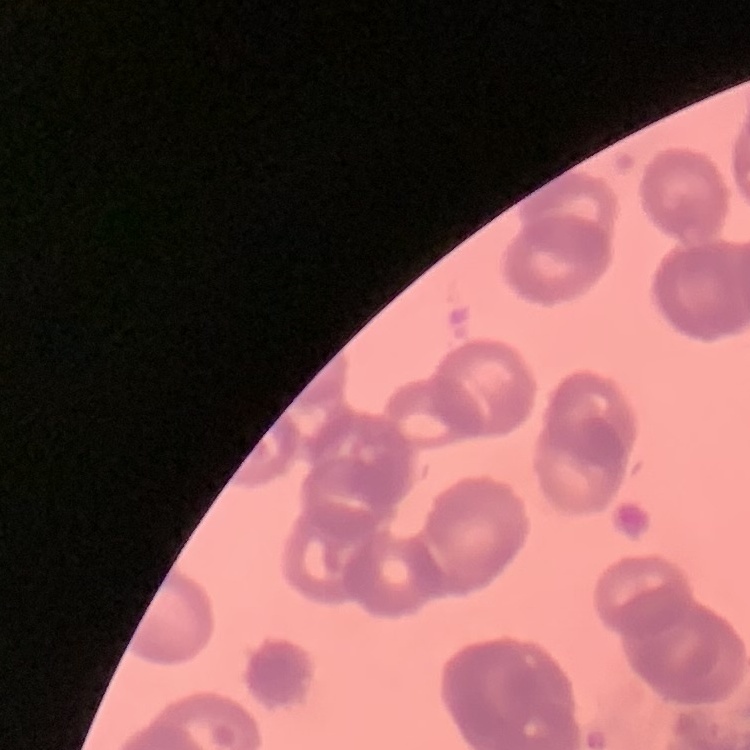

The red blood cells exhibit rouleaux formation. Thin blood smear. Field's or Giemsa stain. Square crop of a larger photomicrograph.